Locate every Plasmodium parasite.
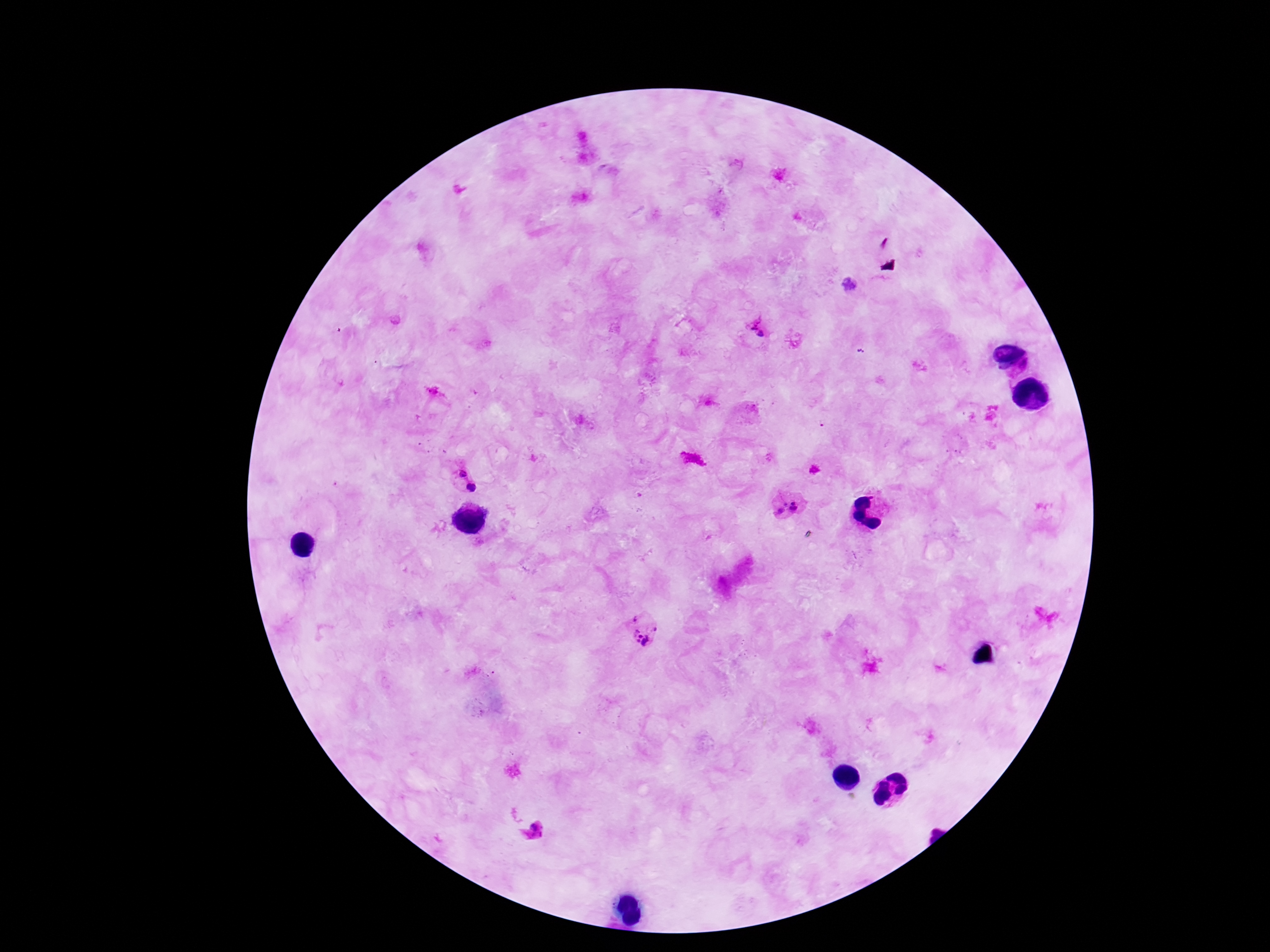
Approximate centers as (x, y) in pixels.
Plasmodium parasites: (757, 327), (1023, 368), (459, 470), (473, 487), (781, 500), (795, 507), (780, 512), (644, 629), (535, 833).

image size = 1270×952 pixels
magnification = 100x
capture = smartphone camera through the microscope eyepiece
stain = Giemsa
patient malaria status = positive
preparation = thick blood film
field of view = single